Assess this cell for malaria.
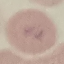
It is uninfected.

image type = automatically extracted cell patch, resized to 64 × 64 pixels
stain = Giemsa
capture = smartphone through the microscope eyepiece
preparation = thin blood film